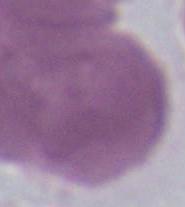
Summary:
  - Magnification: 1000x
  - Modality: micrograph
  - Identification: red blood cell